State which cell type is depicted.
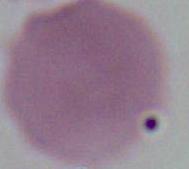
An erythrocyte.

Micrograph. 1000x magnification.